Comment on the morphology of the red blood cells.
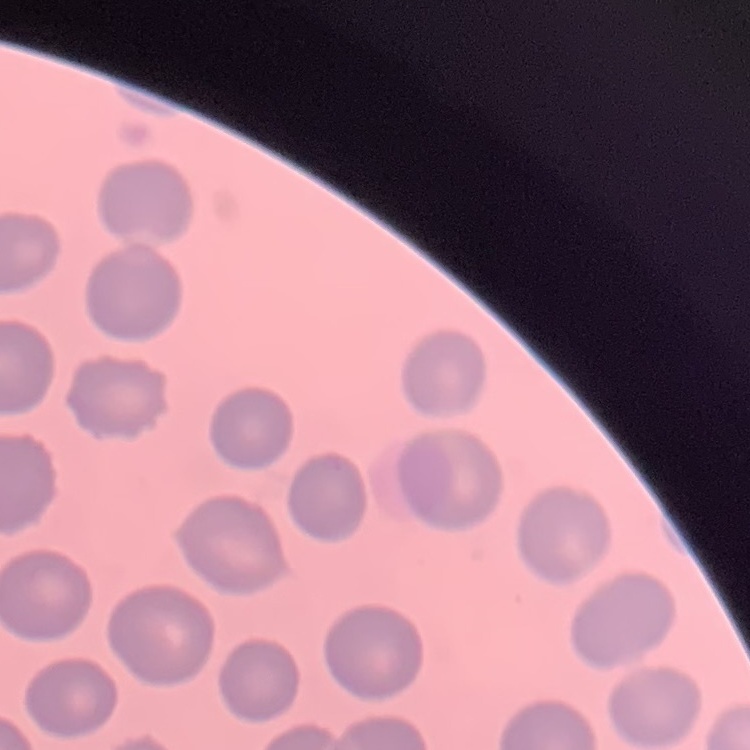

They show no rouleaux formation.

One tile cut from a larger photomicrograph. Field's or Giemsa stain. Thin blood film.